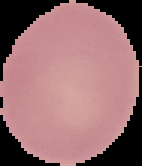
From a thin blood film. Cell region segmented out of the field of view; the surrounding area is masked to black. Image is 142×166 pixels. Result: no malaria parasites detected.